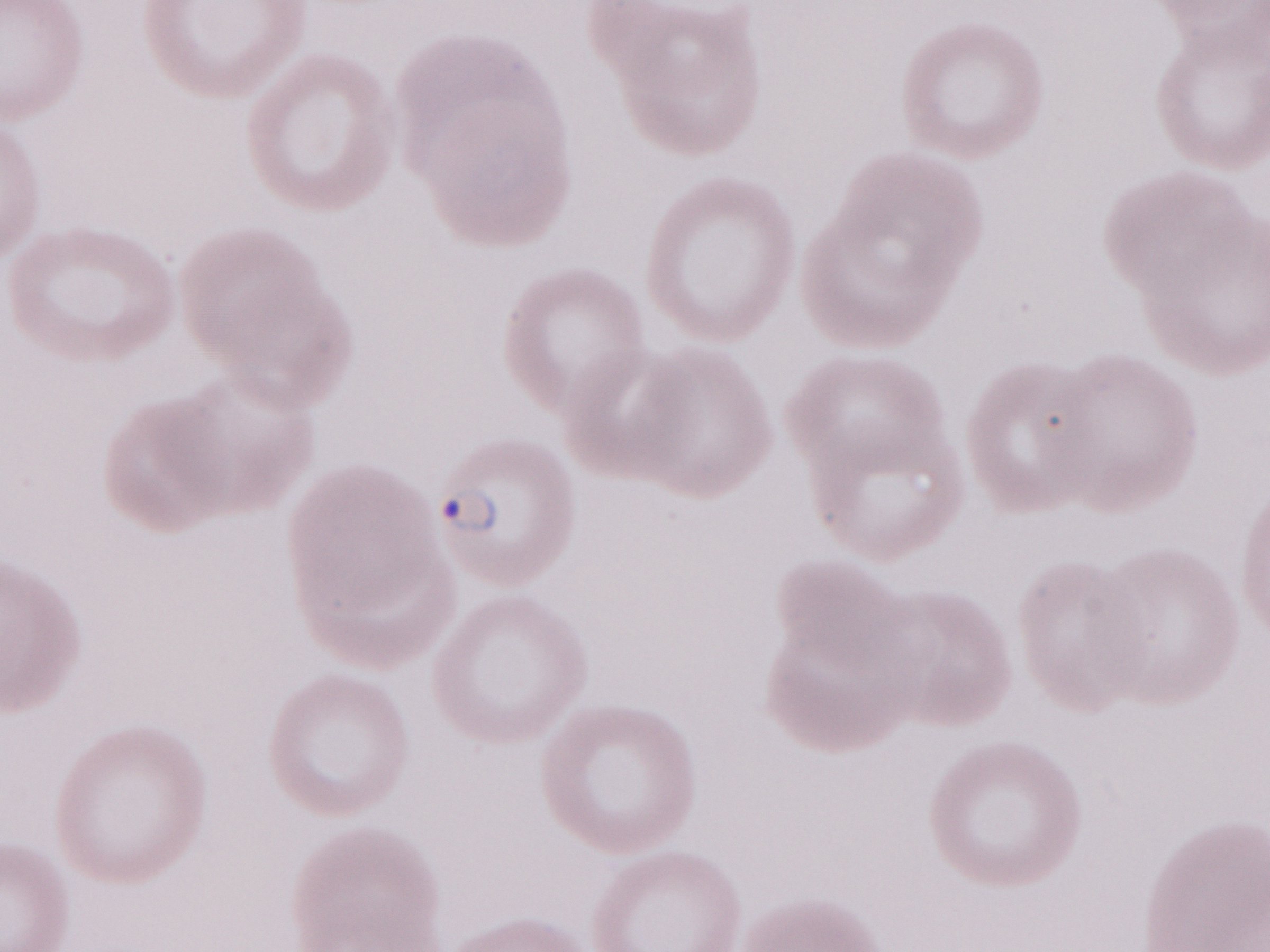
Thin peripheral-blood smear. Image is 1270×952 pixels. One field of this slide. Olympus BX43 microscope and DP73 digital camera. May-Grünwald-Giemsa-stained preparation. Malaria diagnosis (patient-level): positive. Magnification: 1,000x.